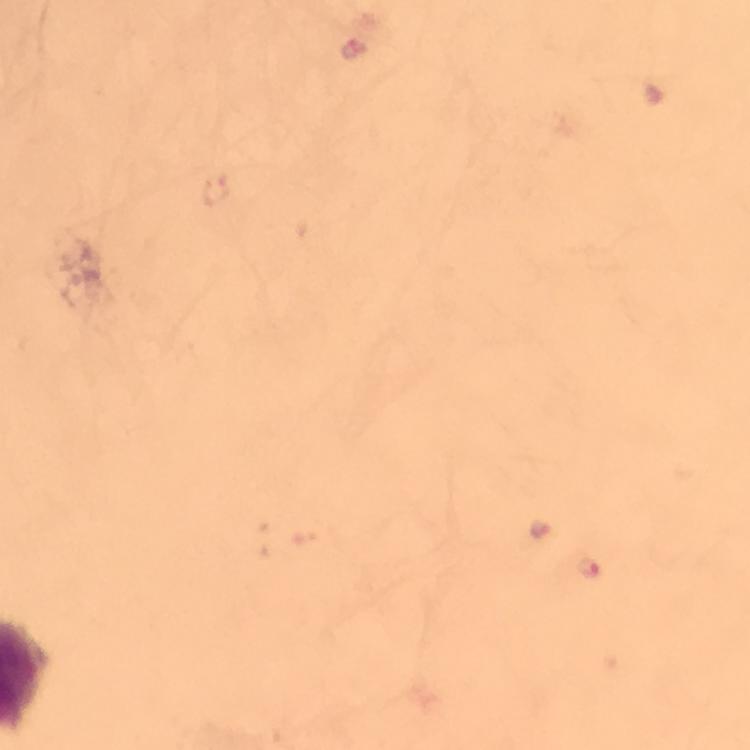

Approximate object centers, in pixels from the top-left corner. Plasmodium parasite locations: (x=352, y=48), (x=219, y=192), (x=539, y=530), (x=590, y=566). From a malaria diagnostic workup. Immersion oil was used. Thick smear. At 100x magnification. Image is 750×750 pixels. A crop from one field of view. Photographed with a smartphone mounted on the microscope. Giemsa-stained preparation.